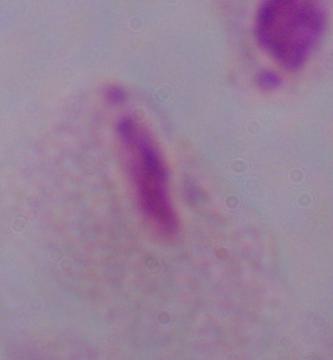

magnification: 1000x
modality: photomicrograph
identification: trichomonad